Assess this cell for malaria.
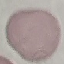
It is uninfected.

Acquired by smartphone through the microscope eyepiece. Cell patch, automatically extracted from a larger field of view and resized to 64 × 64 pixels. Giemsa stain. Thin blood smear.